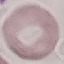

Result: negative for malaria parasites. Cell patch, automatically extracted from a larger field of view and resized to 64 × 64 pixels. Thin blood film. Photographed with a smartphone camera at the microscope eyepiece. Giemsa stain.